Name the parasite shown.
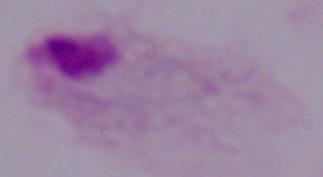
A trichomonad.

Summary:
  - Modality: micrograph
  - Magnification: 1000x